Assess the morphology of the erythrocytes.
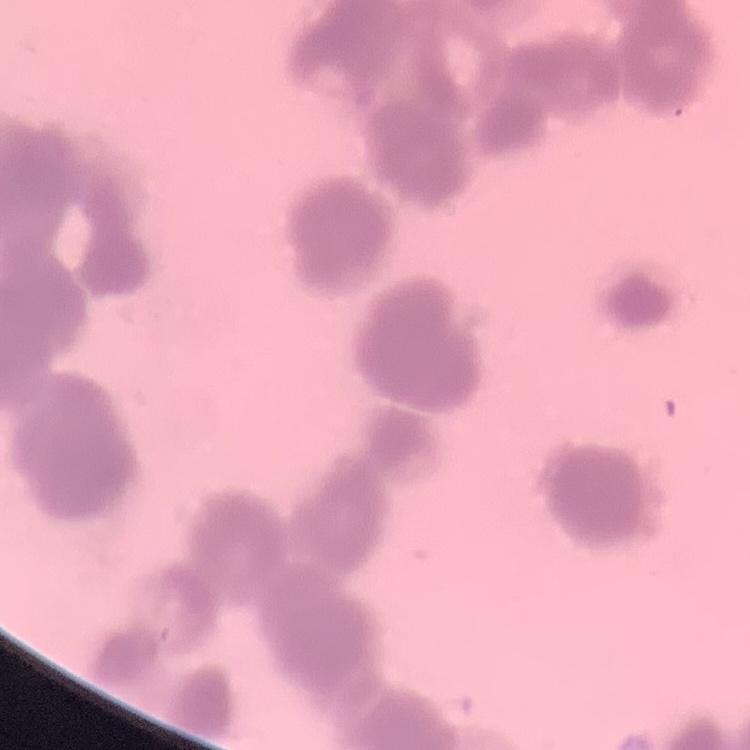
Rouleaux formation.

Summary:
  - Image type: one tile cut from a larger photomicrograph
  - Stain: Field's or Giemsa
  - Preparation: thin peripheral smear